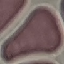
Summary:
  - Result: no malaria parasites detected
  - Image type: cell patch, automatically extracted from a larger field of view and resized to 64 × 64 pixels
  - Stain: Giemsa
  - Preparation: thin blood film
  - Capture: smartphone camera at the microscope eyepiece